Locate and identify every blood parasite.
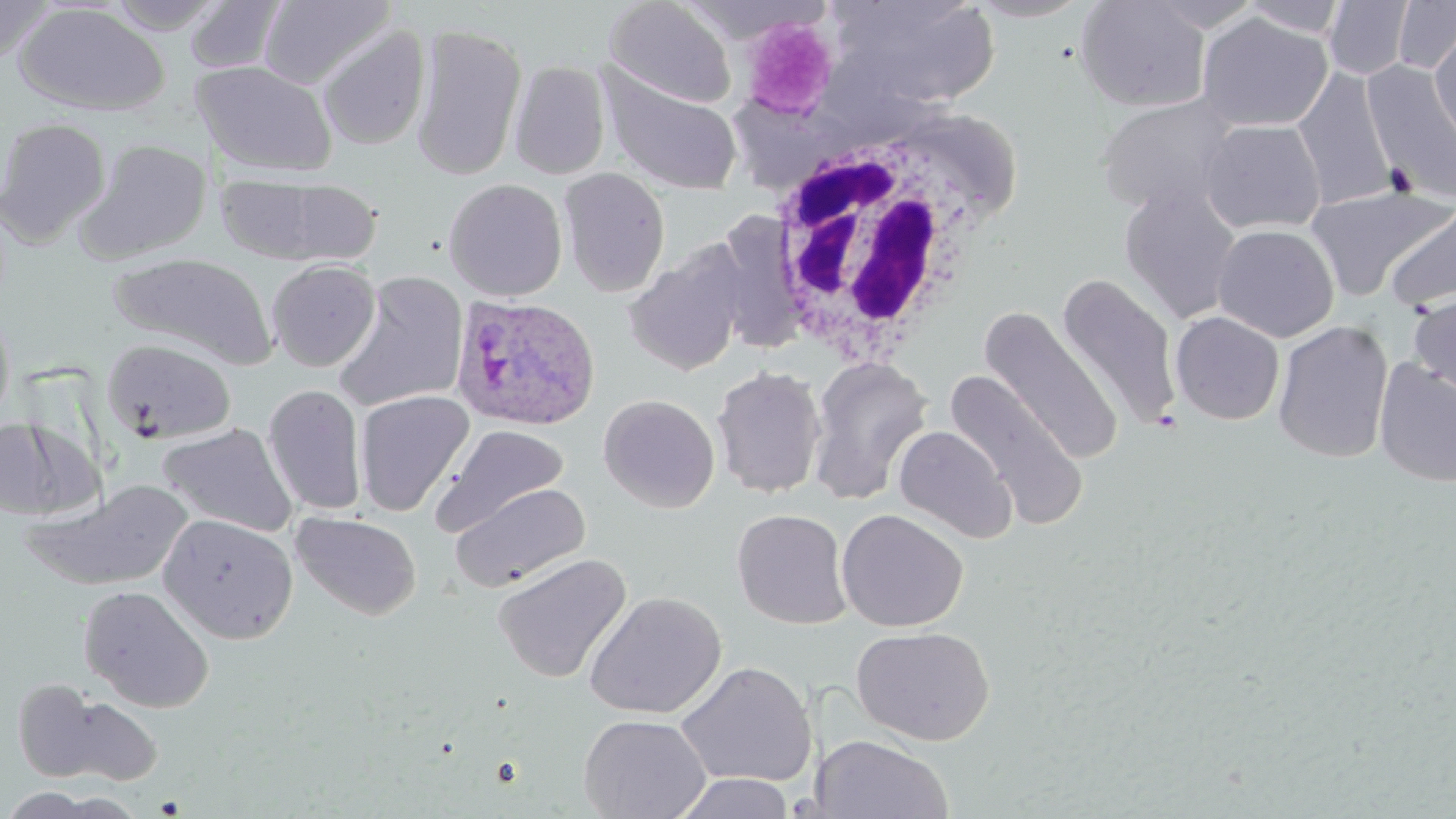
Approximate bounding boxes as (x1, y1, x2, y2) in pixels.
Plasmodium ovale-infected red blood cells: (452, 294, 600, 432).
No Plasmodium falciparum, Plasmodium malariae, Plasmodium vivax, Babesia divergens, or Trypanosoma brucei observed.

Summary:
  - Uninfected red blood cell locations: (102, 0, 230, 33), (604, 0, 737, 108), (825, 0, 1001, 113), (964, 0, 1092, 22), (1141, 0, 1265, 32), (1239, 0, 1351, 38), (1323, 0, 1416, 80), (1, 1, 56, 67), (184, 1, 288, 74), (258, 1, 395, 91), (1075, 1, 1212, 112), (1392, 1, 1456, 75), (13, 3, 170, 117), (1197, 13, 1332, 133), (410, 22, 527, 183), (317, 23, 431, 152), (1429, 30, 1456, 146), (193, 60, 337, 178), (509, 61, 611, 180), (1363, 62, 1456, 205), (596, 63, 743, 197), (1292, 65, 1400, 210), (1096, 95, 1242, 216), (0, 116, 112, 246), (1199, 119, 1326, 235), (78, 139, 212, 262), (559, 167, 671, 297), (215, 172, 382, 266), (443, 178, 568, 301), (1305, 184, 1453, 302), (1120, 187, 1242, 324), (1382, 197, 1456, 313), (1213, 224, 1339, 343), (624, 241, 749, 377), (106, 252, 278, 369), (266, 259, 381, 372), (334, 270, 469, 412), (1056, 273, 1183, 429), (1409, 291, 1456, 406), (0, 301, 16, 431), (978, 307, 1123, 465), (1170, 311, 1285, 425), (1272, 320, 1394, 464), (102, 339, 236, 446), (807, 357, 932, 504), (1373, 358, 1456, 488), (711, 365, 827, 499), (944, 370, 1090, 530), (263, 383, 367, 516), (354, 389, 475, 516), (599, 394, 720, 513), (0, 417, 88, 520), (158, 422, 298, 538), (434, 424, 569, 536), (893, 425, 1018, 543), (29, 480, 195, 590), (451, 482, 590, 592), (836, 508, 968, 632), (732, 509, 853, 629), (291, 511, 422, 621), (159, 513, 298, 644), (492, 552, 632, 684), (78, 585, 215, 713), (583, 591, 726, 719), (852, 625, 995, 746), (675, 660, 818, 788), (37, 689, 164, 786), (578, 714, 710, 819), (811, 733, 955, 818), (673, 772, 795, 818)
  - White blood cell locations: (757, 121, 1003, 374)
  - Platelet locations: (741, 16, 838, 119)
  - Slide-level diagnosis: Plasmodium ovale
  - Image size: 1456×819 pixels
  - Modality: optical microscopy
  - Preparation: thin blood film
  - Field of view: one of a larger specimen
  - Magnification: 1000x
  - Stain: May-Grünwald-Giemsa